Assess the morphology of the erythrocytes.
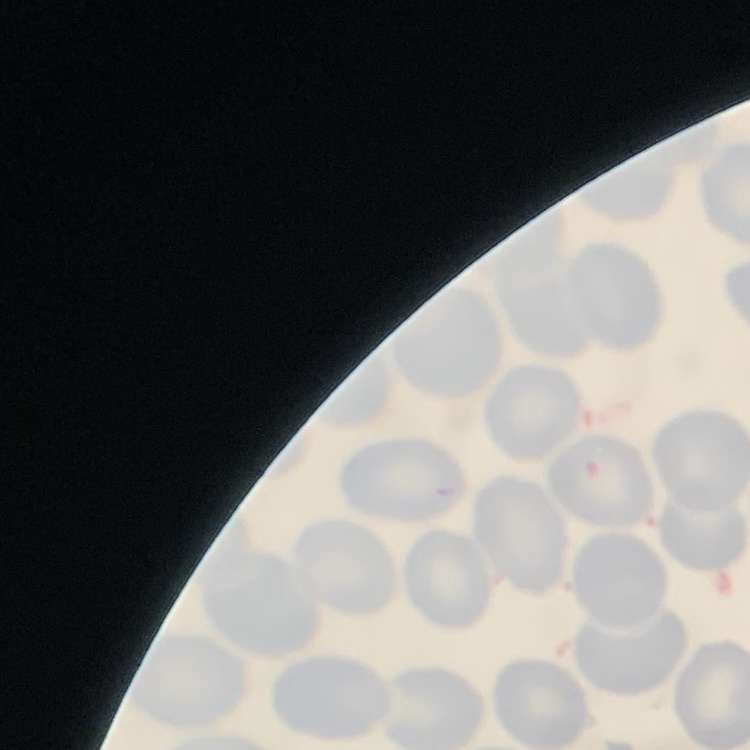
They show no rouleaux formation.

stain: Field's or Giemsa
image_type: one tile cut from a larger photomicrograph
preparation: thin blood film